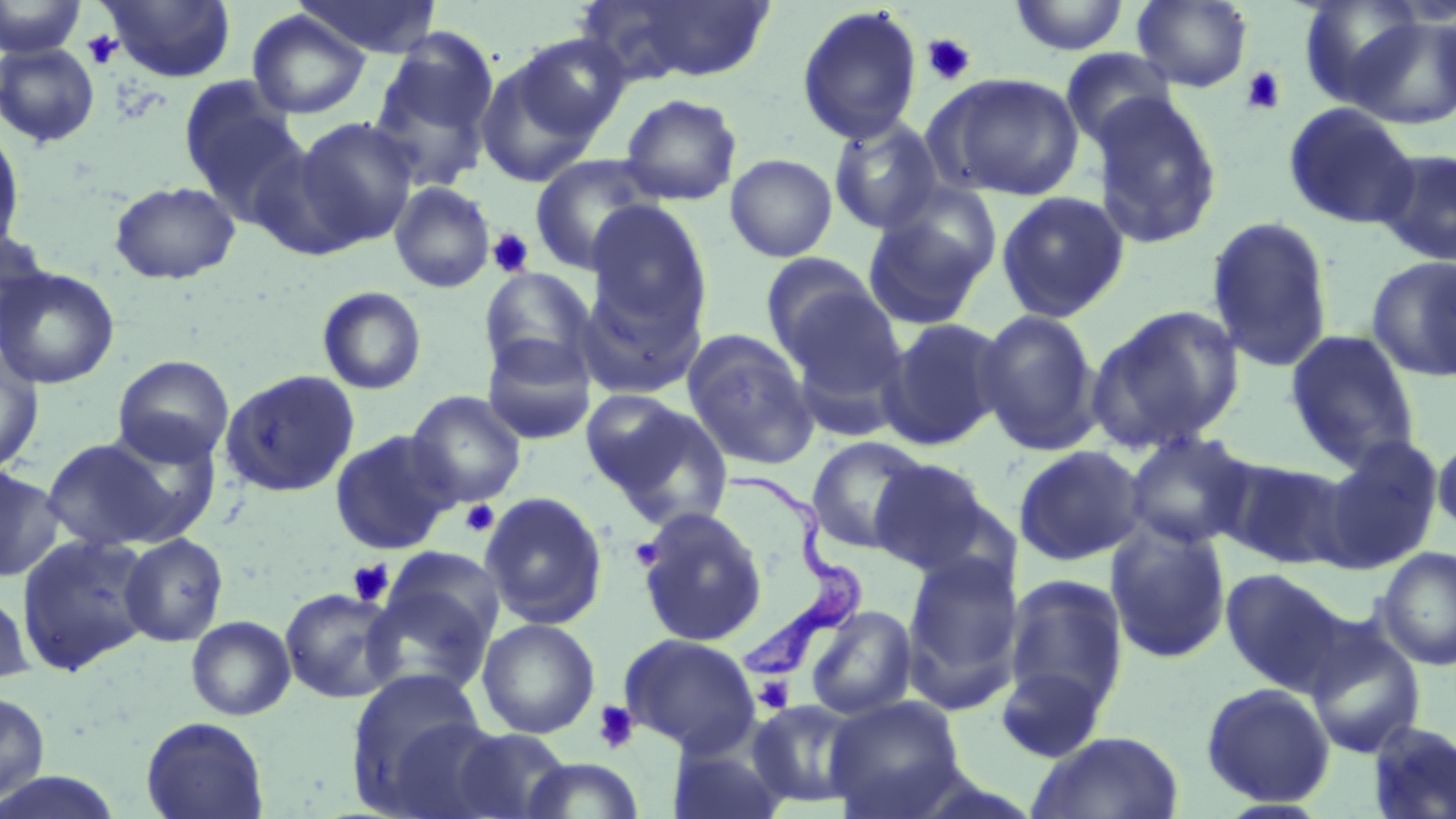

slide-level diagnosis = Trypanosoma brucei
uninfected red blood cell locations = approximate bounding boxes as [x1, y1, x2, y2] in pixels: [1, 0, 88, 59], [101, 0, 235, 82], [294, 0, 442, 58], [1008, 0, 1130, 55], [1132, 0, 1253, 92], [1297, 0, 1426, 108], [587, 1, 777, 83], [796, 5, 924, 145], [247, 10, 370, 119], [1348, 14, 1456, 129], [368, 30, 501, 188], [514, 33, 630, 141], [0, 42, 101, 148], [1060, 48, 1178, 153], [475, 56, 599, 188], [930, 73, 1084, 201], [180, 85, 310, 225], [619, 93, 743, 206], [1089, 94, 1223, 250], [1282, 103, 1420, 229], [295, 117, 420, 247], [827, 117, 946, 235], [0, 124, 25, 255], [247, 142, 367, 261], [1374, 148, 1456, 265], [529, 153, 663, 275], [725, 153, 838, 262], [108, 180, 241, 285], [389, 181, 496, 293], [996, 191, 1129, 323], [862, 193, 999, 332], [585, 200, 712, 336], [1206, 216, 1334, 373], [0, 227, 51, 350], [761, 253, 881, 361], [1366, 256, 1456, 382], [0, 266, 121, 389], [479, 267, 597, 380], [578, 276, 706, 401], [317, 286, 427, 395], [780, 287, 909, 410], [1087, 304, 1246, 453], [974, 308, 1103, 455], [879, 316, 1009, 450], [1284, 329, 1421, 470], [682, 330, 819, 470], [482, 333, 596, 445], [0, 346, 44, 476], [112, 354, 234, 467], [220, 368, 360, 497], [407, 391, 526, 508], [587, 395, 733, 527], [328, 429, 461, 555], [1123, 431, 1257, 551], [1433, 431, 1456, 536], [806, 436, 932, 555], [41, 437, 187, 552], [1321, 439, 1442, 571], [1013, 444, 1146, 567], [1216, 455, 1352, 570], [869, 458, 1000, 577], [0, 465, 65, 583], [479, 491, 608, 630], [635, 506, 768, 647], [1105, 522, 1232, 664], [15, 532, 154, 675], [119, 533, 228, 647], [1376, 546, 1456, 671], [903, 550, 1023, 705], [362, 564, 500, 695], [1220, 568, 1346, 691], [1003, 575, 1129, 717], [0, 586, 34, 686], [280, 587, 400, 703], [805, 605, 918, 721], [185, 615, 296, 721], [477, 618, 600, 738], [1304, 628, 1426, 758], [619, 632, 760, 755], [994, 662, 1113, 764], [347, 670, 496, 813], [1200, 681, 1336, 807], [0, 689, 50, 805], [823, 696, 967, 818], [747, 699, 867, 808], [140, 715, 270, 819], [1367, 720, 1456, 818], [447, 727, 575, 819], [1027, 730, 1185, 819], [667, 738, 791, 819], [518, 757, 647, 818]
modality = light microscopy
field of view = single
image size = 1456×819 pixels
platelet locations = approximate bounding boxes as [x1, y1, x2, y2] in pixels: [82, 30, 122, 68], [920, 33, 977, 86], [1240, 66, 1287, 116], [486, 228, 535, 278], [461, 500, 499, 536], [631, 537, 664, 569], [347, 559, 393, 606], [755, 675, 795, 713], [592, 700, 639, 754]
Trypanosoma brucei locations = approximate bounding boxes as [x1, y1, x2, y2] in pixels: [722, 468, 867, 684]
preparation = thin blood film
magnification = 1000x
stain = May-Grünwald-Giemsa